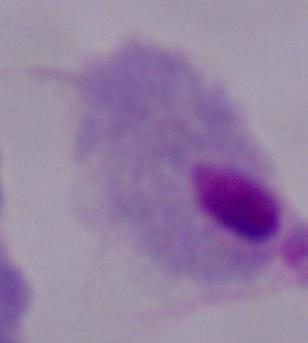
magnification: 1000x
identification: trichomonad
modality: photomicrograph